Name the parasite shown.
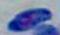
This is Toxoplasma gondii.

magnification: 1000x
modality: photomicrograph